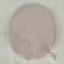
result = no malaria parasites seen
capture = smartphone camera at the microscope eyepiece
preparation = thin blood smear
image type = automatically extracted cell patch, resized to 64 × 64 pixels
stain = Giemsa